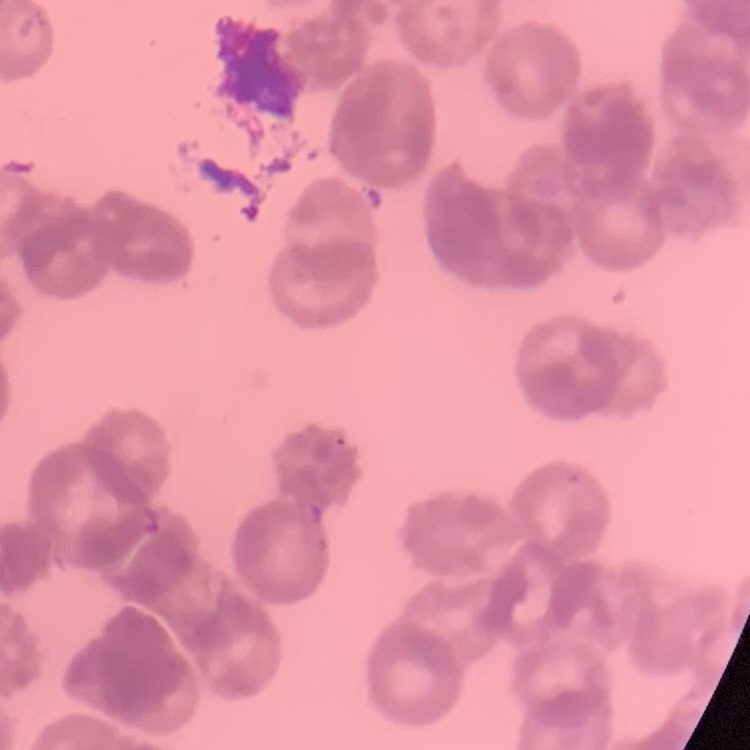

{
  "erythrocyte_morphology": "rouleaux formation",
  "image_type": "one tile cut from a larger photomicrograph",
  "preparation": "thin peripheral smear",
  "stain": "Field's or Giemsa"
}